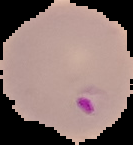
image type = segmented cell region with the area outside set to black
preparation = thin blood film
image size = 133×145 pixels
malaria status = parasitized